Classify this cell by malaria status.
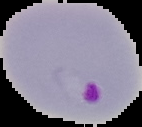
It is parasitized.

From a thin blood film. Image is 142×127 pixels. Cell region segmented out of the field of view; the surrounding area is masked to black.